Give the position of every Plasmodium parasite and every leukocyte.
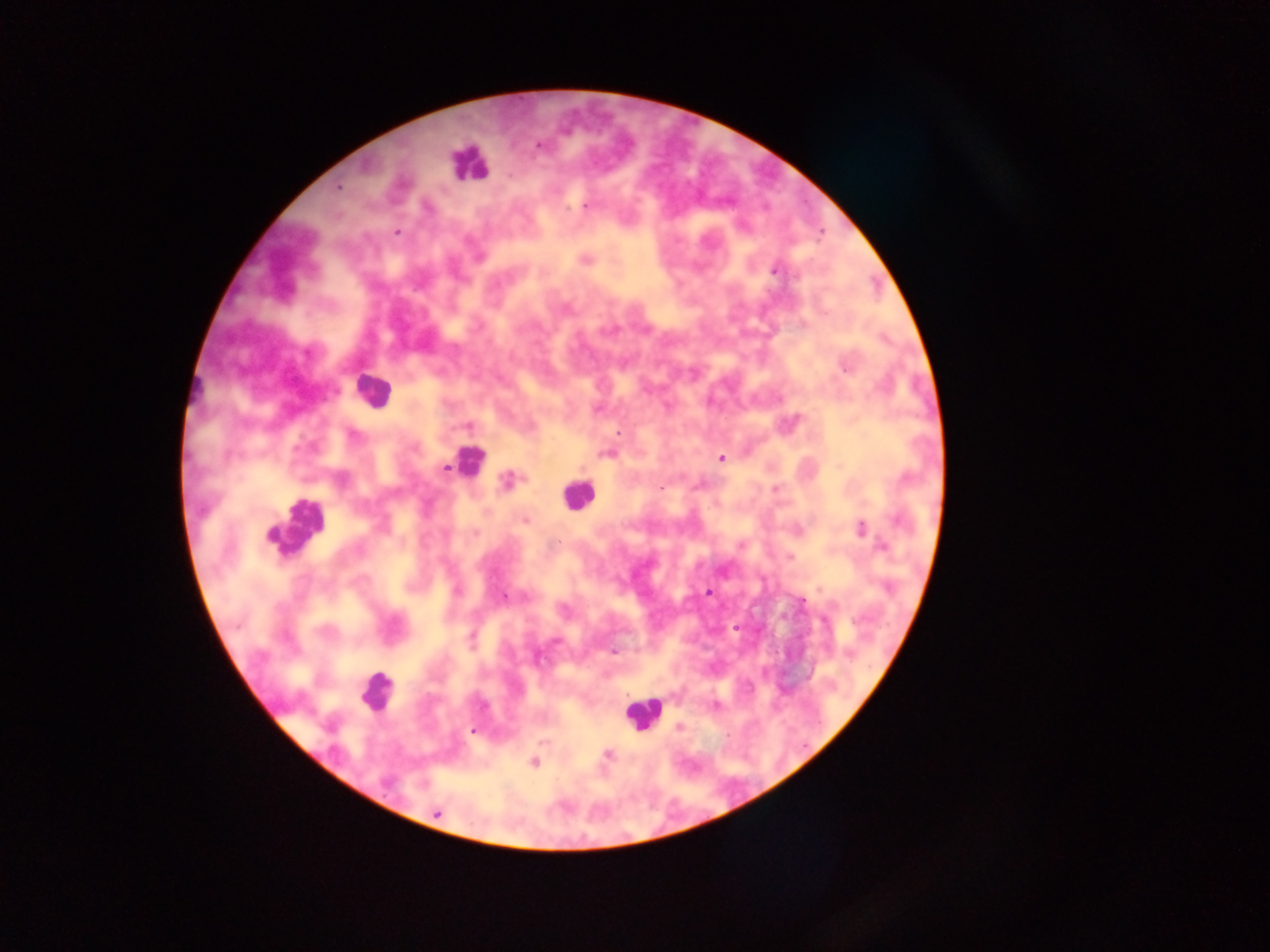

Approximate centers as x y in pixels.
Plasmodium parasites: 539 145; 339 187; 585 206; 397 232; 478 258; 585 260; 775 272; 845 369; 618 433; 607 453; 721 459; 445 468; 507 482; 661 488; 775 489; 525 521; 861 528; 475 532; 881 546; 790 557; 456 590; 708 593; 504 597; 471 637; 556 642; 614 652; 849 656; 538 657; 679 727; 472 731; 608 754; 535 763; 437 813.
Leukocytes: 468 164; 371 391; 469 461; 577 496; 295 527; 376 691; 642 712.

One field of view. Thick blood smear. Sample from Ghana. Image is 1270×952 pixels. Mobile-phone photograph taken through the microscope.